Comment on the morphology of the red blood cells.
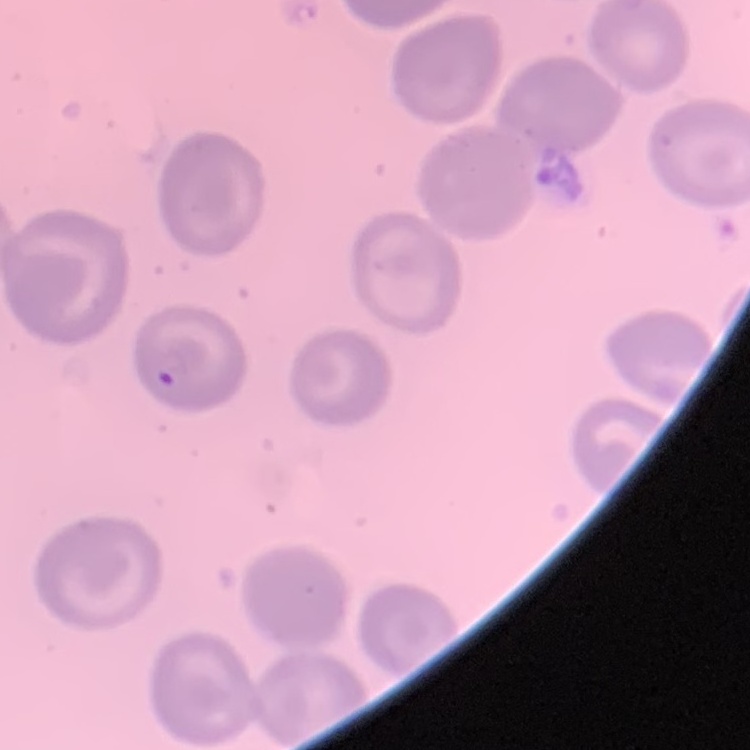

No rouleaux formation.

Summary:
  - Image type: one tile cut from a larger photomicrograph
  - Stain: Field's or Giemsa
  - Preparation: thin blood smear